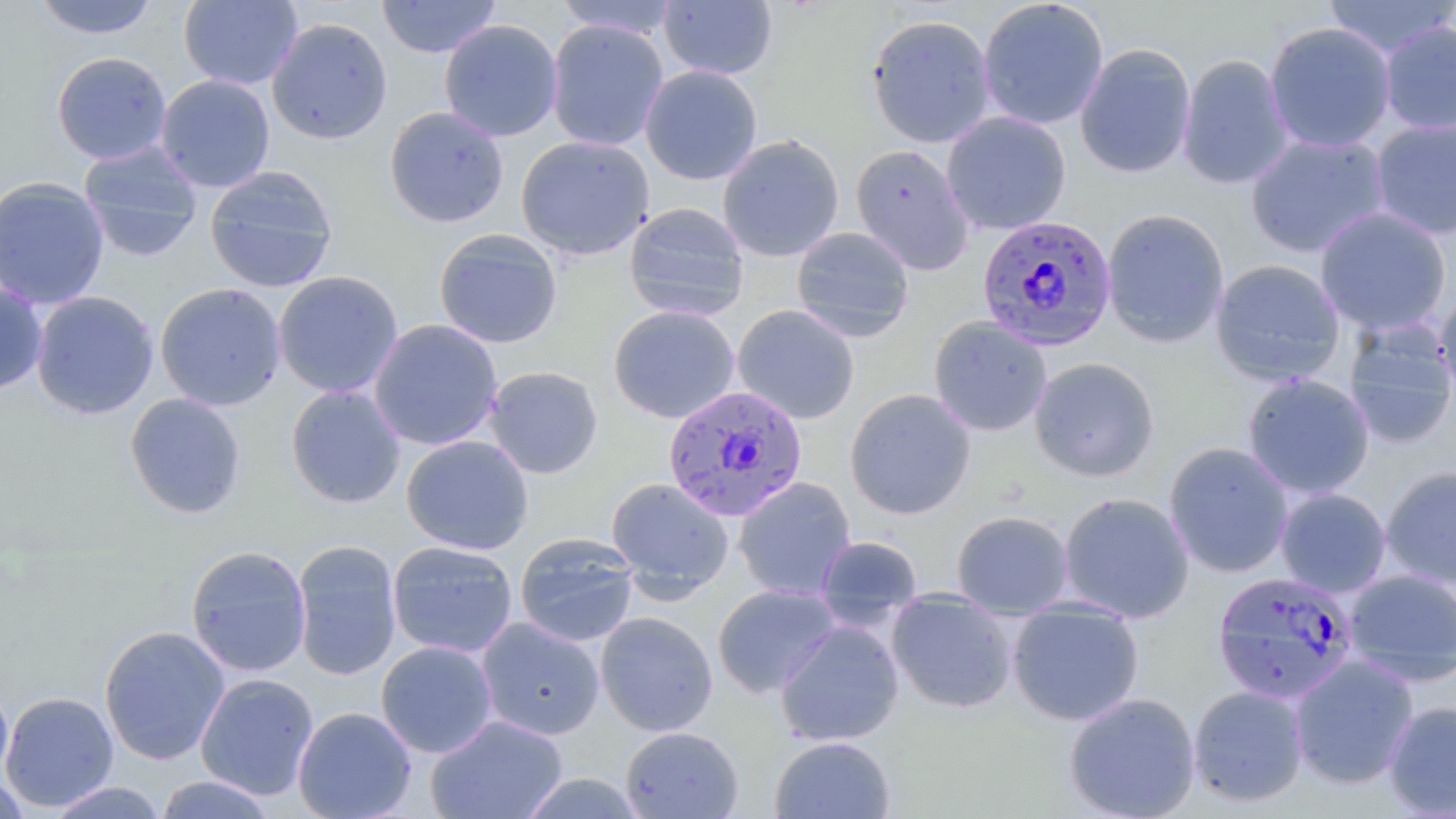
Approximate bounding boxes as [x1, y1, x2, y2] in pixels. Plasmodium falciparum-infected red blood cell locations: [976, 215, 1117, 351], [662, 384, 807, 521], [1212, 571, 1360, 705]. Uninfected red blood cell locations: [32, 0, 160, 40], [178, 0, 303, 90], [376, 0, 502, 58], [554, 0, 681, 39], [659, 0, 778, 80], [977, 0, 1109, 130], [1322, 0, 1456, 59], [866, 14, 995, 147], [266, 17, 393, 145], [439, 19, 563, 142], [546, 19, 669, 152], [1379, 21, 1456, 136], [1264, 22, 1396, 153], [1075, 43, 1197, 179], [51, 51, 172, 165], [1177, 54, 1294, 189], [640, 65, 763, 186], [155, 74, 276, 193], [384, 106, 509, 228], [941, 112, 1072, 235], [1370, 118, 1456, 240], [1245, 133, 1390, 258], [515, 135, 655, 260], [717, 135, 845, 262], [78, 142, 204, 261], [850, 144, 974, 274], [204, 165, 339, 293], [0, 175, 110, 310], [624, 202, 750, 321], [1314, 207, 1452, 337], [1101, 208, 1230, 348], [791, 227, 914, 342], [433, 228, 563, 349], [1210, 259, 1346, 387], [273, 270, 403, 398], [0, 281, 48, 396], [154, 282, 287, 411], [30, 290, 159, 419], [1435, 292, 1456, 403], [608, 305, 740, 424], [732, 305, 860, 424], [928, 316, 1053, 436], [368, 319, 503, 451], [1342, 320, 1456, 447], [1029, 357, 1160, 481], [483, 365, 603, 479], [1241, 372, 1376, 499], [285, 384, 406, 508], [844, 388, 977, 519], [124, 393, 247, 519], [401, 434, 534, 555], [1164, 442, 1294, 578], [1380, 465, 1456, 589], [733, 476, 857, 601], [605, 477, 735, 600], [1275, 487, 1392, 598], [1058, 491, 1195, 623], [951, 510, 1074, 618], [515, 533, 639, 647], [815, 535, 923, 629], [292, 540, 402, 681], [387, 540, 518, 658], [186, 545, 312, 677], [1343, 569, 1456, 683], [712, 583, 841, 698], [885, 590, 1019, 714], [1007, 599, 1145, 726], [595, 611, 718, 736], [476, 617, 605, 741], [775, 619, 904, 747], [98, 625, 230, 765], [376, 640, 498, 759], [1289, 654, 1419, 790], [195, 673, 319, 800], [0, 681, 14, 792], [1188, 685, 1309, 807], [1, 691, 119, 812], [1063, 692, 1201, 819], [1383, 701, 1456, 817], [292, 706, 417, 819], [425, 714, 568, 818], [619, 726, 743, 818], [769, 735, 896, 818], [518, 772, 647, 818], [0, 774, 33, 818], [154, 775, 279, 818], [46, 781, 169, 818]. Slide-level diagnosis: Plasmodium falciparum. Single field of view. Thin blood smear. 1000x magnification. May-Grünwald-Giemsa stain. Optical microscopy. Image is 1456×819 pixels.